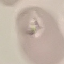

result = no malaria parasites detected
image type = cell patch, automatically extracted from a larger field of view and resized to 64 × 64 pixels
capture = smartphone camera at the microscope eyepiece
preparation = thin smear
stain = Giemsa